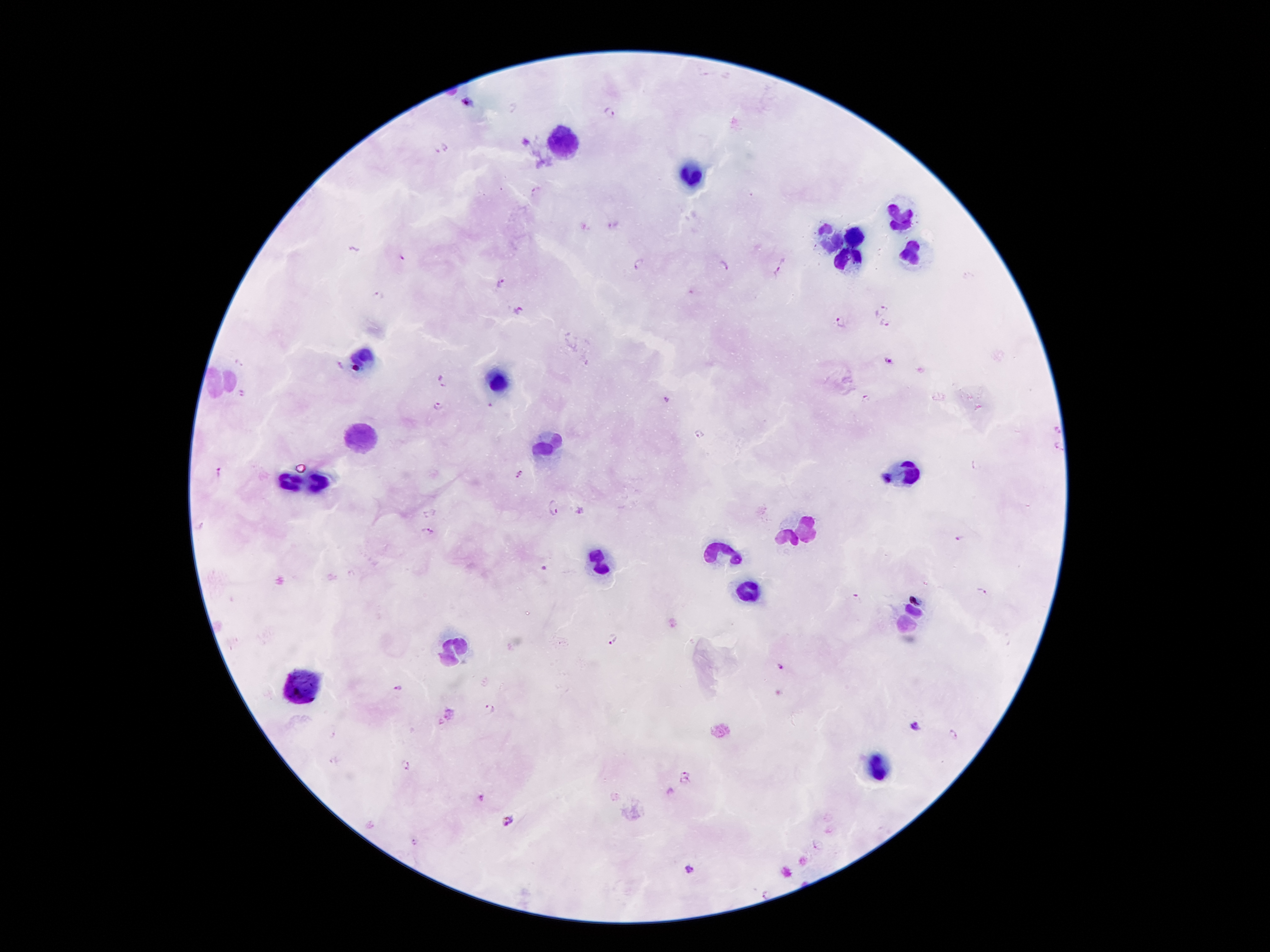
{
  "preparation": "thick blood smear",
  "image_size": "1270×952 pixels",
  "plasmodium_parasite_locations": "approximate centers as [x, y] in pixels: [468, 102], [512, 108], [611, 112], [447, 147], [435, 151], [535, 190], [401, 258], [640, 262], [724, 265], [779, 271], [500, 284], [381, 294], [521, 310], [883, 310], [840, 322], [885, 325], [890, 360], [239, 364], [445, 383], [241, 393], [867, 398], [666, 400], [440, 405], [490, 406], [1059, 429], [700, 434], [1058, 447], [218, 472], [519, 474], [887, 479], [553, 509], [580, 510], [428, 513], [427, 530], [959, 539], [544, 568], [984, 589], [915, 597], [856, 598], [613, 639], [782, 666], [396, 687], [490, 706], [917, 724], [332, 734], [953, 734], [407, 765], [686, 771], [686, 781], [482, 797], [510, 819], [414, 841], [689, 867], [764, 893]",
  "leukocyte_locations": "approximate centers as [x, y] in pixels: [568, 138], [693, 176], [897, 217], [856, 235], [831, 240], [908, 251], [847, 260], [363, 356], [218, 381], [500, 381], [359, 440], [545, 444], [906, 469], [288, 480], [318, 483], [808, 527], [786, 538], [727, 556], [601, 564], [750, 593], [917, 612], [904, 626], [456, 649], [304, 683], [878, 770]",
  "capture": "smartphone through the microscope eyepiece",
  "field_of_view": "single",
  "magnification": "100x",
  "stain": "Giemsa",
  "patient_malaria_status": "positive for Plasmodium falciparum"
}